Describe the morphology of the erythrocytes.
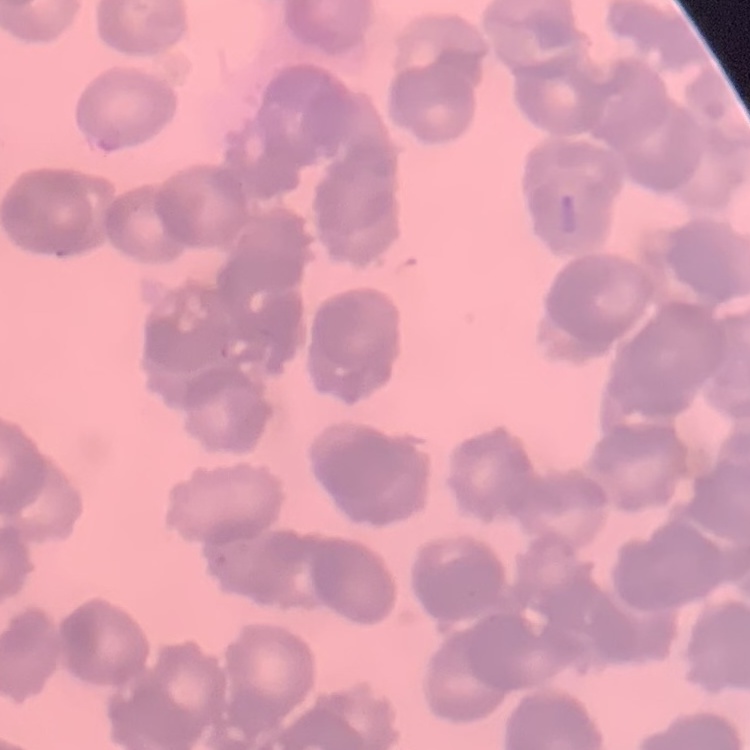

They show rouleaux formation.

{
  "stain": "Field's or Giemsa",
  "image_type": "one tile cut from a larger photomicrograph",
  "preparation": "thin blood film"
}